State the blood parasite species.
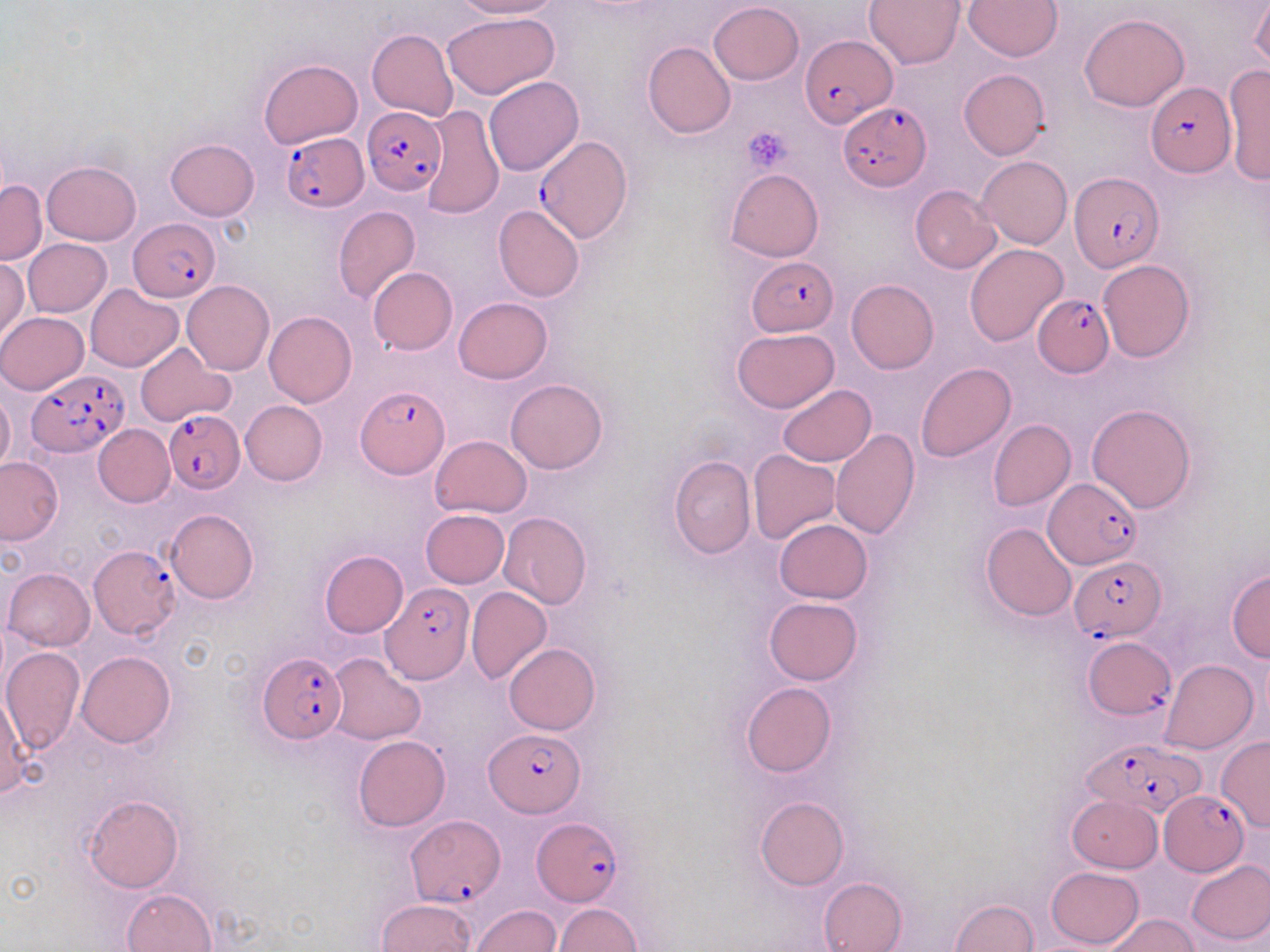
Plasmodium falciparum.

platelet locations = approximate bounding boxes as (x1, y1, x2, y2) in pixels: (743, 126, 794, 172)
image size = 1270×952 pixels
field of view = single
preparation = thin blood film
modality = optical microscopy
uninfected red blood cell locations = approximate bounding boxes as (x1, y1, x2, y2) in pixels: (453, 0, 561, 19), (864, 0, 965, 69), (964, 1, 1062, 60), (709, 2, 805, 85), (1251, 2, 1270, 75), (653, 10, 793, 107), (442, 12, 559, 100), (1079, 13, 1189, 112), (367, 28, 457, 120), (642, 42, 736, 139), (258, 59, 362, 147), (1222, 63, 1270, 186), (958, 69, 1051, 159), (484, 75, 583, 176), (419, 103, 504, 219), (165, 138, 259, 220), (976, 156, 1072, 249), (42, 161, 140, 245), (726, 168, 824, 263), (0, 179, 46, 264), (910, 184, 1002, 273), (494, 205, 585, 301), (334, 207, 419, 304), (23, 239, 111, 318), (964, 244, 1069, 347), (0, 257, 29, 344), (1098, 260, 1195, 363), (368, 267, 458, 355), (846, 279, 938, 374), (182, 280, 274, 375), (85, 283, 183, 371), (454, 297, 552, 383), (0, 311, 88, 395), (264, 311, 357, 407), (732, 328, 840, 413), (135, 343, 235, 427), (916, 363, 1015, 461), (505, 377, 608, 474), (778, 384, 876, 466), (0, 390, 15, 472), (240, 400, 327, 485), (1086, 403, 1197, 512), (988, 419, 1077, 511), (93, 424, 175, 507), (830, 427, 920, 539), (430, 434, 533, 517), (748, 449, 840, 544), (668, 455, 755, 558), (0, 457, 64, 545), (165, 508, 258, 604), (420, 509, 509, 588), (499, 512, 590, 609), (774, 520, 873, 603), (980, 521, 1077, 621), (318, 550, 409, 638), (3, 567, 95, 651), (1227, 570, 1270, 662), (465, 586, 552, 684), (763, 597, 863, 685), (504, 643, 600, 735), (2, 647, 85, 756), (76, 651, 176, 749), (328, 653, 426, 744), (1161, 659, 1258, 754), (741, 682, 836, 776), (353, 736, 450, 831), (1217, 737, 1270, 829), (84, 794, 183, 892), (1067, 794, 1161, 872), (755, 796, 848, 890), (1185, 858, 1270, 946), (1045, 866, 1143, 949), (818, 876, 907, 952), (122, 888, 217, 952), (375, 898, 476, 952), (950, 898, 1038, 951), (553, 903, 642, 951), (471, 905, 561, 951), (1106, 914, 1200, 952)
stain = May-Grünwald-Giemsa
Plasmodium falciparum-infected red blood cell locations = approximate bounding boxes as (x1, y1, x2, y2) in pixels: (801, 33, 895, 127), (1145, 81, 1236, 179), (840, 100, 931, 190), (361, 106, 447, 195), (282, 132, 369, 211), (534, 134, 633, 243), (1070, 172, 1162, 272), (129, 219, 221, 302), (747, 256, 840, 336), (1032, 296, 1114, 374), (28, 369, 129, 457), (355, 385, 451, 478), (164, 411, 245, 492), (1044, 479, 1142, 569), (88, 545, 181, 640), (1070, 556, 1165, 641), (381, 583, 473, 684), (1084, 638, 1174, 718), (256, 650, 347, 745), (484, 730, 585, 815), (1084, 739, 1208, 823), (1160, 790, 1249, 874), (406, 814, 503, 907), (532, 818, 623, 908)
magnification = 1000x